State which cell type is depicted.
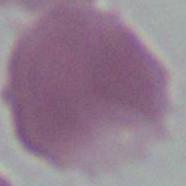
This is an erythrocyte.

magnification = 1000x
modality = micrograph